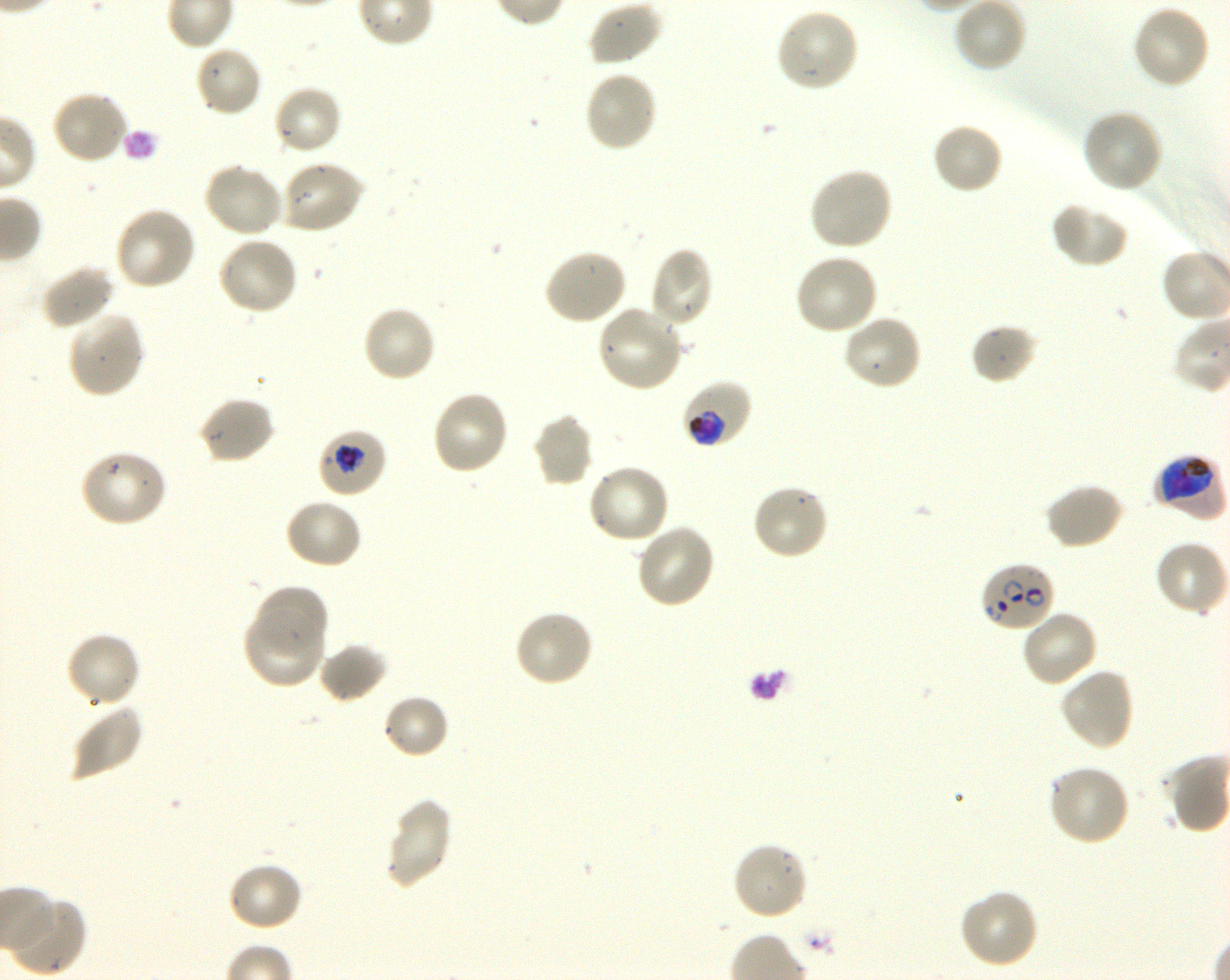
Approximate bounding rectangles given as corner coordinates in pixels from the top-left. Not every red blood cell is marked. A life-cycle stage — or a range of stages, where the recorded stages span more than one — follows each staged infected red blood cell. Locations of uninfected red blood cells: (x1=586, y1=0, x2=663, y2=67), (x1=954, y1=0, x2=1027, y2=72), (x1=1132, y1=4, x2=1211, y2=89), (x1=775, y1=7, x2=860, y2=93), (x1=193, y1=45, x2=263, y2=118), (x1=583, y1=71, x2=659, y2=153), (x1=272, y1=84, x2=344, y2=157), (x1=51, y1=90, x2=130, y2=165), (x1=1080, y1=108, x2=1164, y2=194), (x1=931, y1=121, x2=1003, y2=196), (x1=279, y1=160, x2=365, y2=234), (x1=203, y1=162, x2=285, y2=239), (x1=807, y1=167, x2=893, y2=252), (x1=1051, y1=201, x2=1130, y2=268), (x1=113, y1=207, x2=197, y2=292), (x1=216, y1=236, x2=299, y2=316), (x1=649, y1=247, x2=715, y2=329), (x1=542, y1=248, x2=627, y2=325), (x1=794, y1=253, x2=880, y2=337), (x1=40, y1=265, x2=116, y2=331), (x1=362, y1=305, x2=437, y2=384), (x1=596, y1=305, x2=686, y2=393), (x1=67, y1=311, x2=144, y2=398), (x1=842, y1=313, x2=924, y2=391), (x1=970, y1=322, x2=1039, y2=385), (x1=430, y1=389, x2=510, y2=475), (x1=198, y1=396, x2=276, y2=466), (x1=532, y1=414, x2=595, y2=489), (x1=78, y1=449, x2=168, y2=528), (x1=586, y1=464, x2=670, y2=546), (x1=1043, y1=482, x2=1124, y2=549), (x1=750, y1=483, x2=830, y2=561), (x1=284, y1=498, x2=363, y2=570), (x1=635, y1=523, x2=716, y2=610), (x1=1154, y1=540, x2=1228, y2=617), (x1=255, y1=584, x2=329, y2=658), (x1=243, y1=609, x2=324, y2=690), (x1=513, y1=609, x2=594, y2=689), (x1=1020, y1=609, x2=1099, y2=688), (x1=66, y1=631, x2=141, y2=709), (x1=318, y1=642, x2=388, y2=704), (x1=1059, y1=667, x2=1135, y2=751), (x1=382, y1=694, x2=451, y2=760), (x1=69, y1=702, x2=144, y2=781), (x1=1047, y1=764, x2=1131, y2=847), (x1=384, y1=798, x2=454, y2=889), (x1=731, y1=841, x2=809, y2=921), (x1=227, y1=862, x2=303, y2=933), (x1=957, y1=888, x2=1040, y2=969), (x1=6, y1=897, x2=84, y2=975). Locations of infected red blood cells: (x1=679, y1=381, x2=754, y2=448) trophozoite; (x1=316, y1=428, x2=388, y2=498) trophozoite; (x1=1154, y1=454, x2=1225, y2=517) early trophozoite to early schizont; (x1=979, y1=562, x2=1055, y2=634) ring. Life-cycle stages observed: ring, trophozoite. Giemsa-stained preparation. Single field of view. 100x objective under oil immersion, numerical aperture 1.30. Donor blood group O+. Plasmodium falciparum strain 3D7 maintained in shaking in-vitro culture. Image is 1230×980 pixels. Thin blood film.